Identify the parasite.
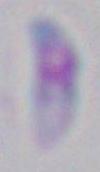
Toxoplasma gondii.

Summary:
  - Modality: micrograph
  - Magnification: 1000x